Comment on the morphology of the red blood cells.
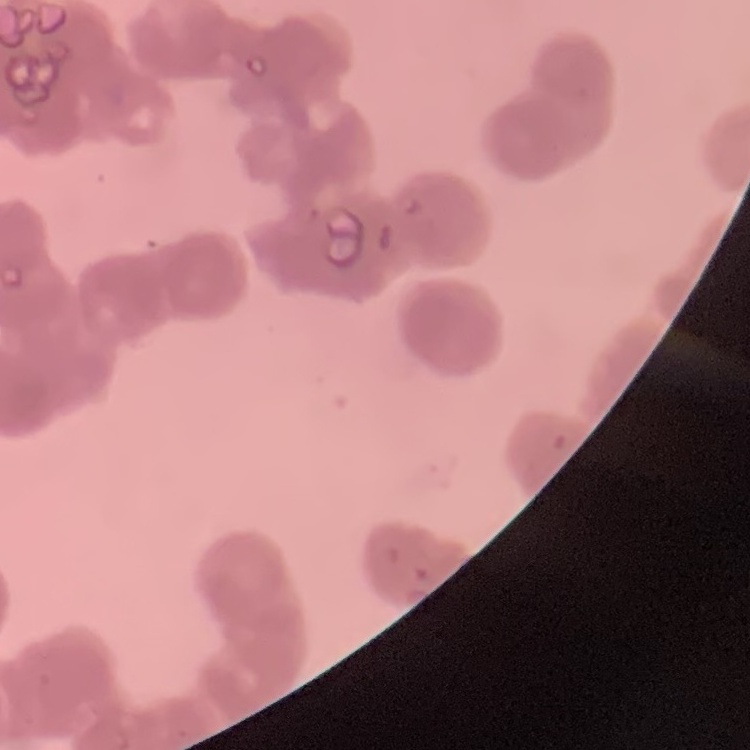
Rouleaux formation.

Summary:
  - Image type: one tile cut from a larger photomicrograph
  - Stain: Field's or Giemsa
  - Preparation: thin blood smear